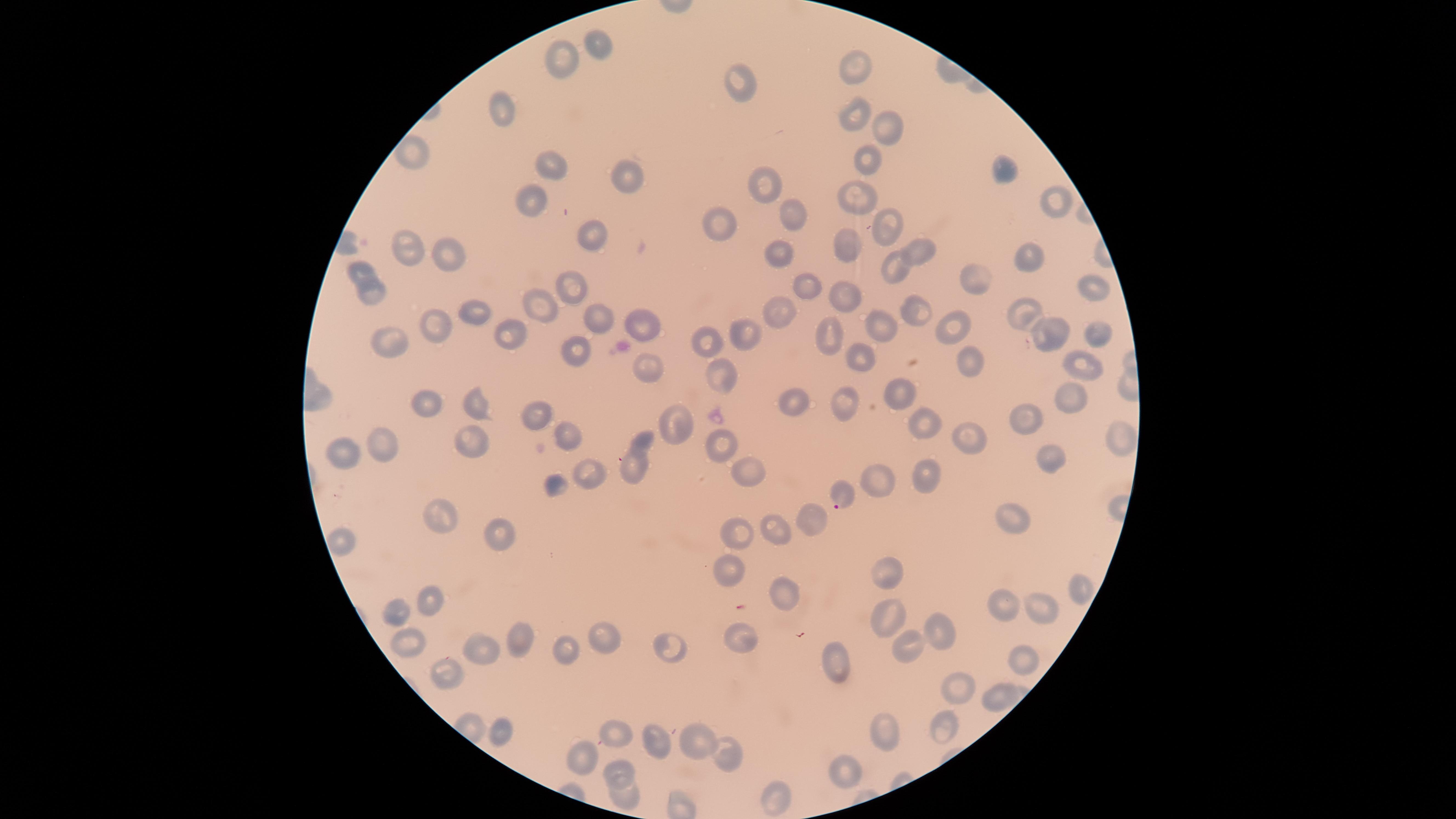
{
  "field_of_view": "single",
  "stain": "Giemsa",
  "species": "Plasmodium falciparum",
  "capture": "smartphone photograph through the microscope eyepiece",
  "presence": "malaria parasites detected",
  "preparation": "thin blood smear",
  "parasitized_red_blood_cells": "approximate marker points as [x, y] in pixels: [842, 493]",
  "uninfected_red_blood_cells": "approximate marker points as [x, y] in pixels: [602, 50], [556, 52], [862, 65], [738, 76], [503, 102], [845, 107], [890, 127], [870, 162], [552, 163], [621, 175], [1002, 175], [765, 180], [860, 195], [1050, 199], [531, 201], [793, 214], [717, 222], [884, 227], [849, 236], [593, 240], [407, 251], [777, 252], [911, 252], [1031, 256], [453, 260], [889, 265], [363, 270], [799, 281], [981, 282], [568, 286], [1087, 289], [377, 292], [841, 299], [539, 306], [789, 306], [915, 308], [473, 313], [1020, 313], [883, 321], [945, 323], [595, 324], [437, 325], [646, 325], [753, 328], [1050, 331], [511, 332], [830, 333], [1096, 335], [708, 341], [401, 343], [571, 353], [963, 358], [860, 359], [650, 364], [1087, 365], [719, 376], [898, 389], [474, 399], [1070, 400], [843, 403], [431, 404], [793, 405], [539, 410], [1027, 421], [679, 425], [924, 425], [561, 432], [1120, 433], [965, 436], [717, 439], [474, 441], [378, 445], [338, 455], [1049, 460], [637, 464], [587, 472], [743, 472], [925, 477], [887, 478], [552, 486], [438, 514], [813, 521], [1014, 523], [778, 526], [737, 531], [501, 538], [344, 545], [889, 569], [732, 572], [1079, 587], [780, 589], [434, 601], [1044, 604], [1001, 606], [397, 610], [888, 615], [940, 626], [514, 634], [740, 638], [601, 640], [671, 645], [412, 646], [908, 646], [483, 648], [563, 649], [1023, 650], [832, 659], [441, 667], [966, 682], [997, 691], [945, 721], [615, 726], [504, 730], [886, 732], [697, 733], [664, 734], [581, 753], [730, 755], [623, 770], [847, 771], [628, 796], [775, 797]",
  "image_size": "1456×819 pixels",
  "visible_region": "circular"
}